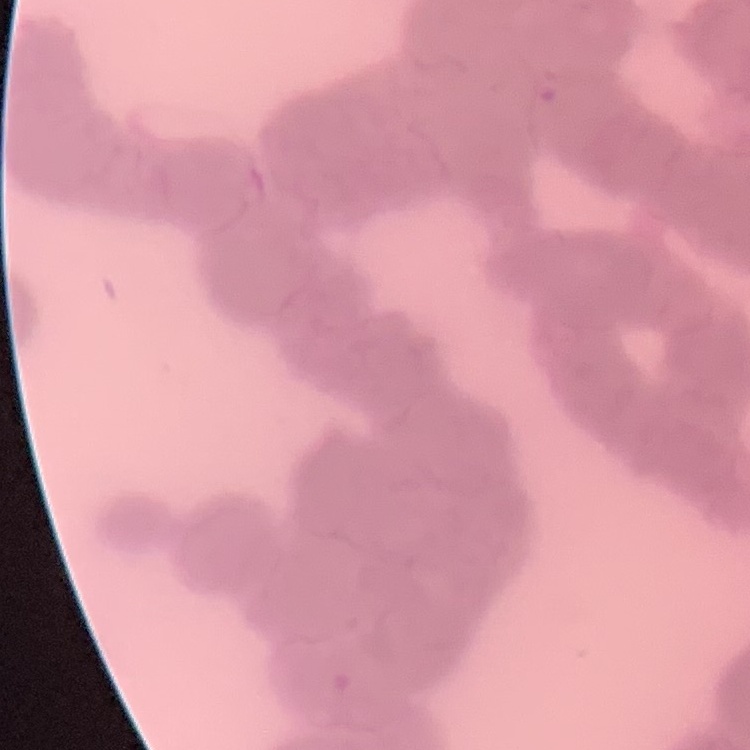 The red blood cells exhibit rouleaux formation. Thin blood smear. Field's or Giemsa stain. Square crop of a larger photomicrograph.